Comment on the morphology of the red blood cells.
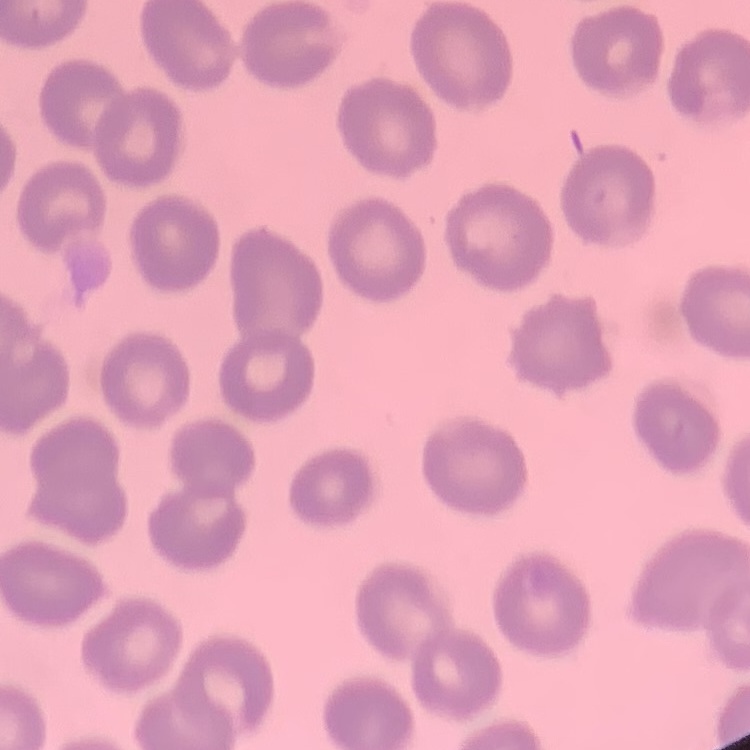

They show no rouleaux formation.

preparation = thin peripheral smear
image type = square crop of a larger photomicrograph
stain = Field's or Giemsa